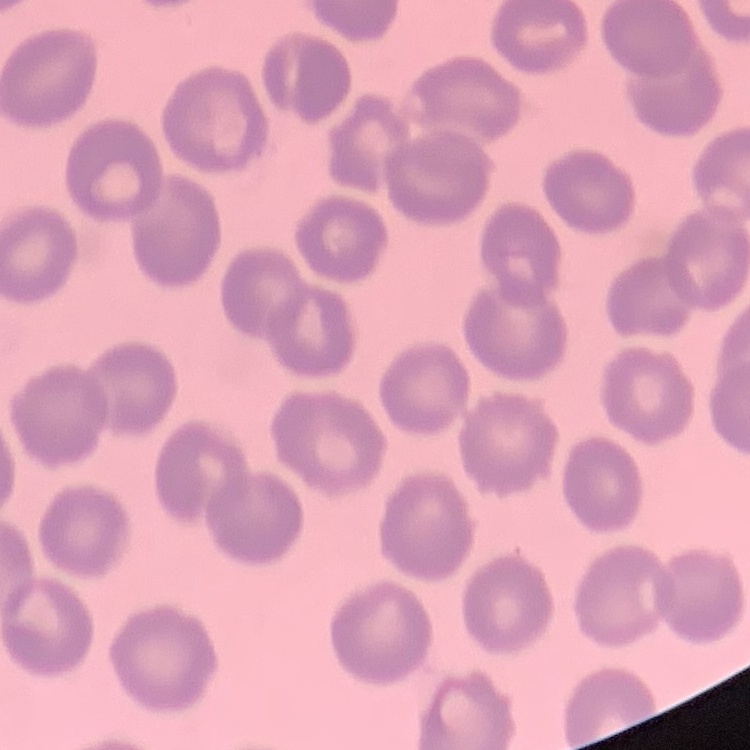
The red blood cells show no rouleaux formation. Field's or Giemsa stain. Square crop of a larger photomicrograph. Thin peripheral smear.